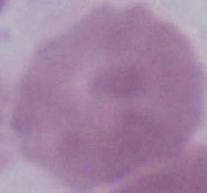
Summary:
  - Magnification: 1000x
  - Modality: photomicrograph
  - Identification: erythrocyte